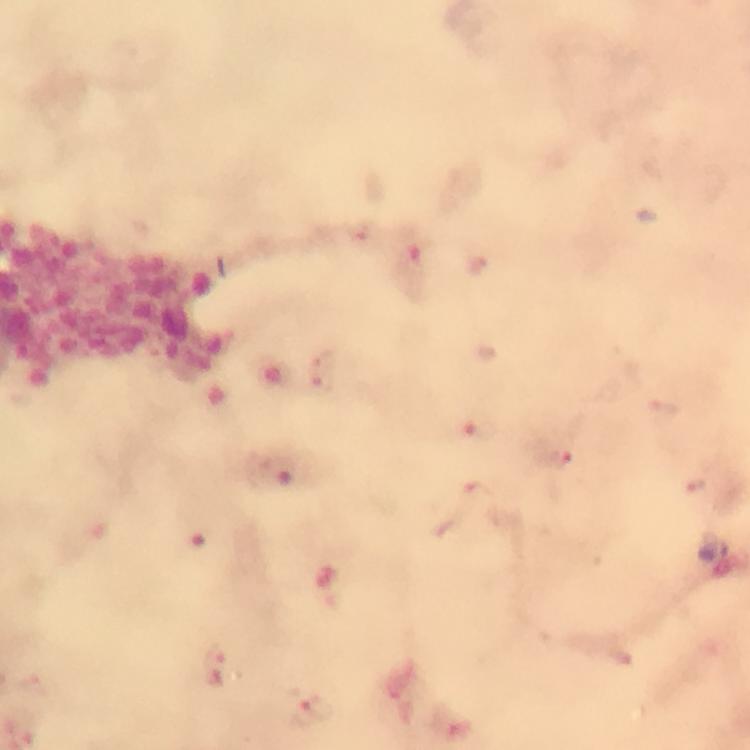

Approximate centers as {x, y} in pixels.
Summary:
  - Malaria parasite locations: {322, 357}, {323, 382}, {480, 426}, {560, 456}, {694, 486}, {214, 652}, {315, 707}
  - Preparation: thick blood film
  - Cropped from: one field of view
  - Stain: Giemsa
  - Image size: 750×750 pixels
  - Capture: smartphone camera through the microscope
  - Immersion oil: used
  - Context: from a malaria diagnostic workup
  - Magnification: 100x